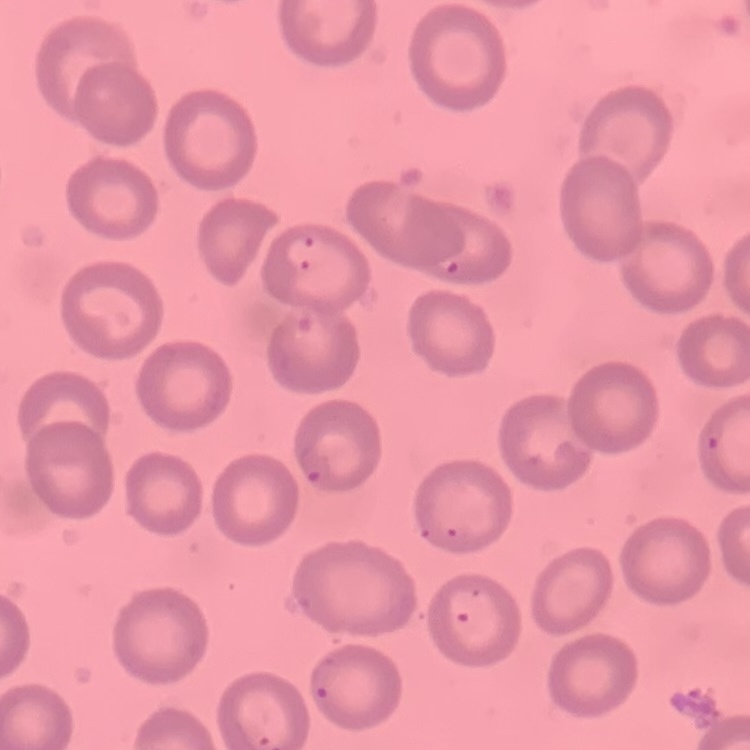 The erythrocytes show no rouleaux formation. Thin blood smear. Stained with either Field's or Giemsa. One tile cut from a larger photomicrograph.